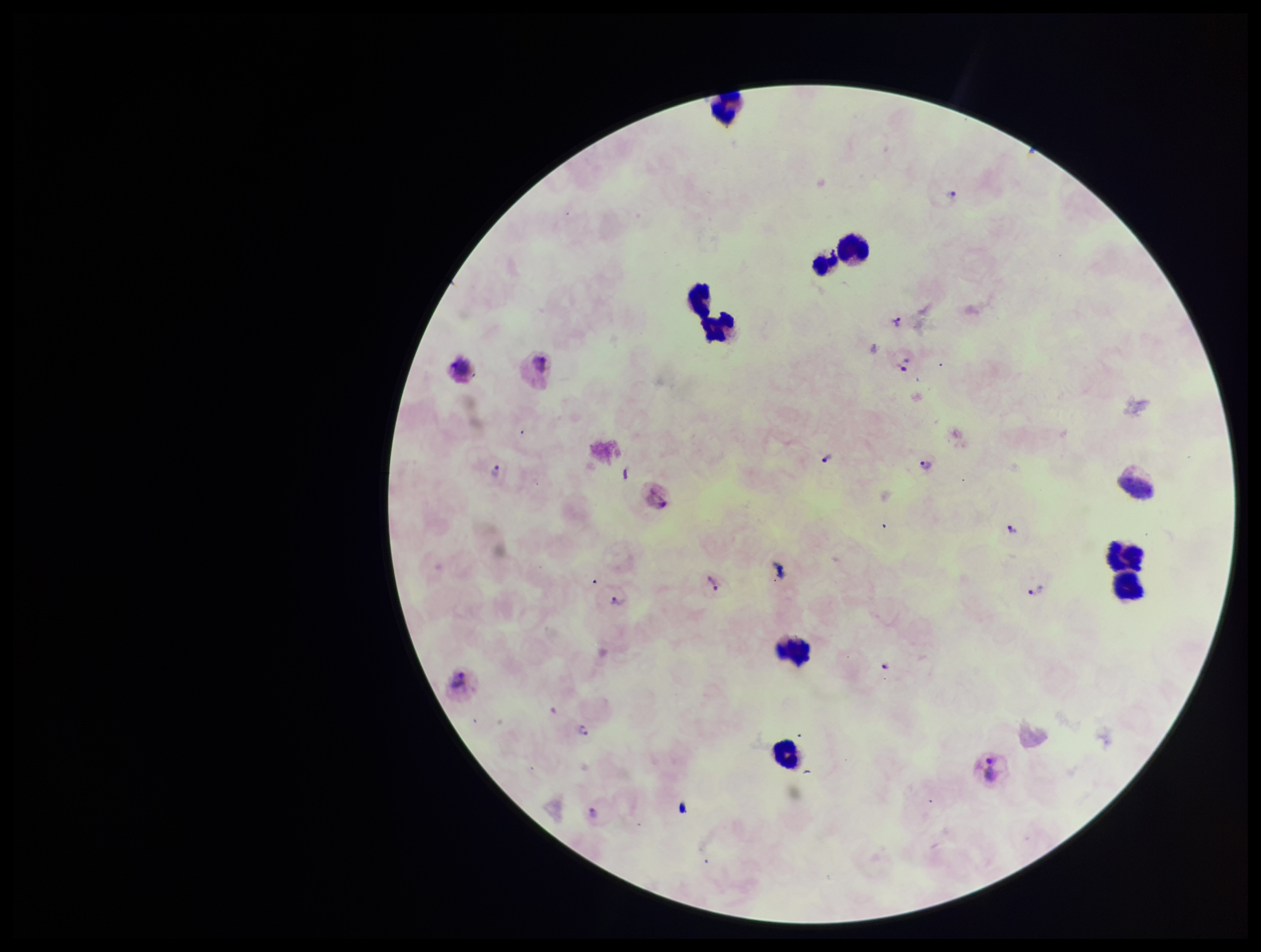

{
  "preparation": "thick",
  "leukocyte_count": 8,
  "image_size": "1261×952 pixels",
  "stain": "Giemsa",
  "plasmodium_parasites": "detected",
  "field_of_view": "one from this slide",
  "species_reported_for_this_patient": "Plasmodium vivax",
  "patient_malaria_status": "infected",
  "parasite_count": 13,
  "capture": "smartphone photograph through the microscope eyepiece"
}